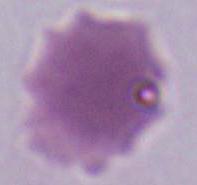 Micrograph. 1000x magnification. An erythrocyte is shown.